Report the malaria status of this cell.
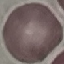

Uninfected.

Thin blood film. Cell patch, automatically extracted from a larger field of view and resized to 64 × 64 pixels. Giemsa stain. Photographed with a smartphone camera at the microscope eyepiece.